Comment on the morphology of the red blood cells.
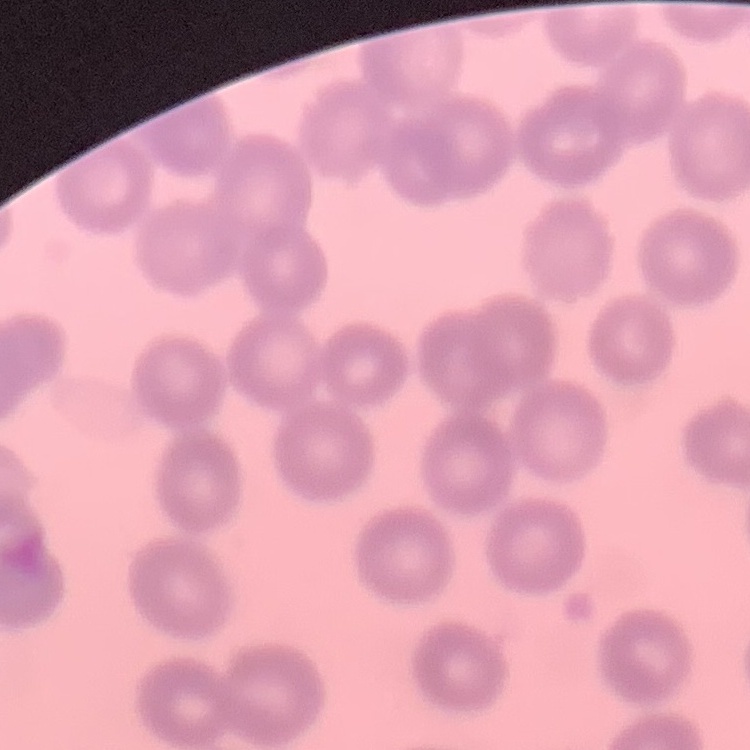

No rouleaux formation.

{
  "stain": "Field's or Giemsa",
  "preparation": "thin peripheral smear",
  "image_type": "square crop of a larger photomicrograph"
}